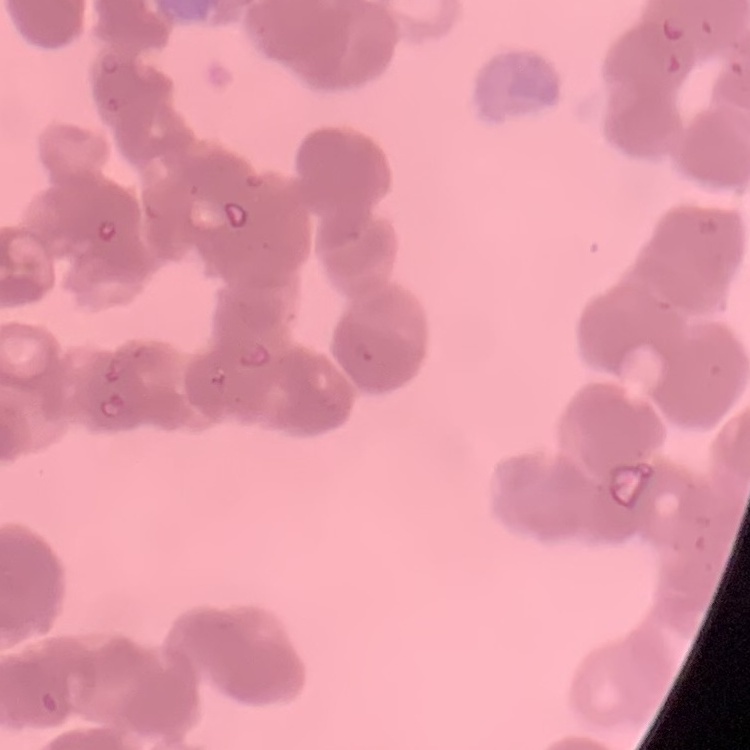

Summary:
  - Erythrocyte morphology: rouleaux formation
  - Stain: Field's or Giemsa
  - Image type: one tile cut from a larger photomicrograph
  - Preparation: thin blood film